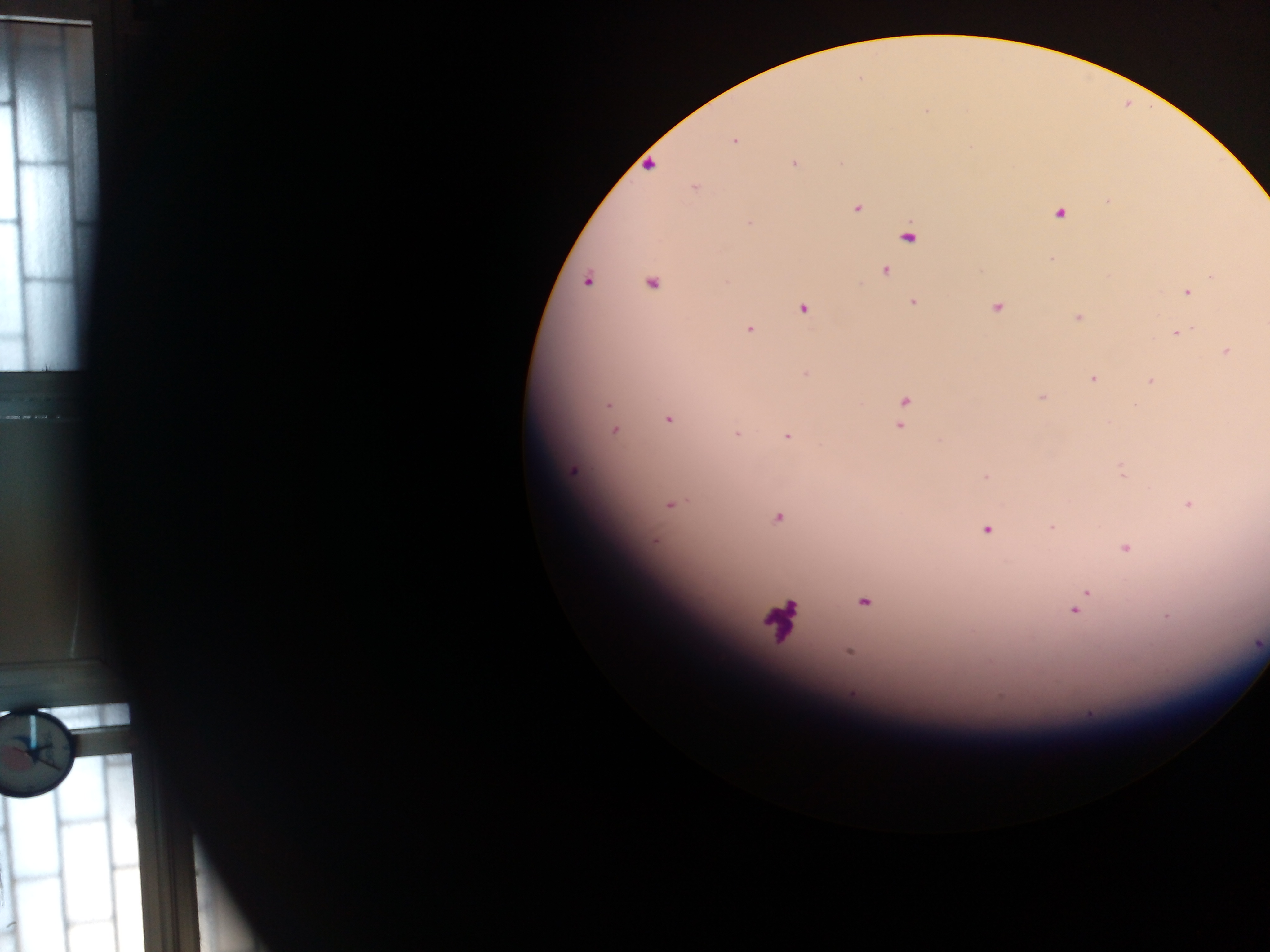
Approximate centers as [x, y] in pixels. Malaria parasite locations: [734, 141], [794, 163], [649, 164], [694, 187], [1108, 201], [856, 207], [1059, 211], [749, 223], [907, 235], [1052, 258], [884, 269], [1212, 274], [587, 280], [725, 281], [651, 282], [1186, 292], [912, 301], [996, 306], [803, 307], [1077, 317], [749, 328], [1177, 332], [1226, 352], [805, 373], [1092, 377], [1150, 381], [1041, 397], [903, 402], [608, 404], [668, 418], [900, 425], [614, 430], [736, 433], [787, 435], [1120, 469], [573, 470], [986, 477], [1186, 503], [670, 504], [777, 517], [1051, 527], [986, 528], [1124, 547], [1086, 592], [863, 601], [1076, 607], [1166, 616], [850, 651], [852, 693]. One field of view. Collected in Ghana. Photographed through a microscope with a mobile-phone camera. Thick blood smear. Image is 1270×952 pixels.